Give the extent of all Plasmodium ovale-infected red blood cells.
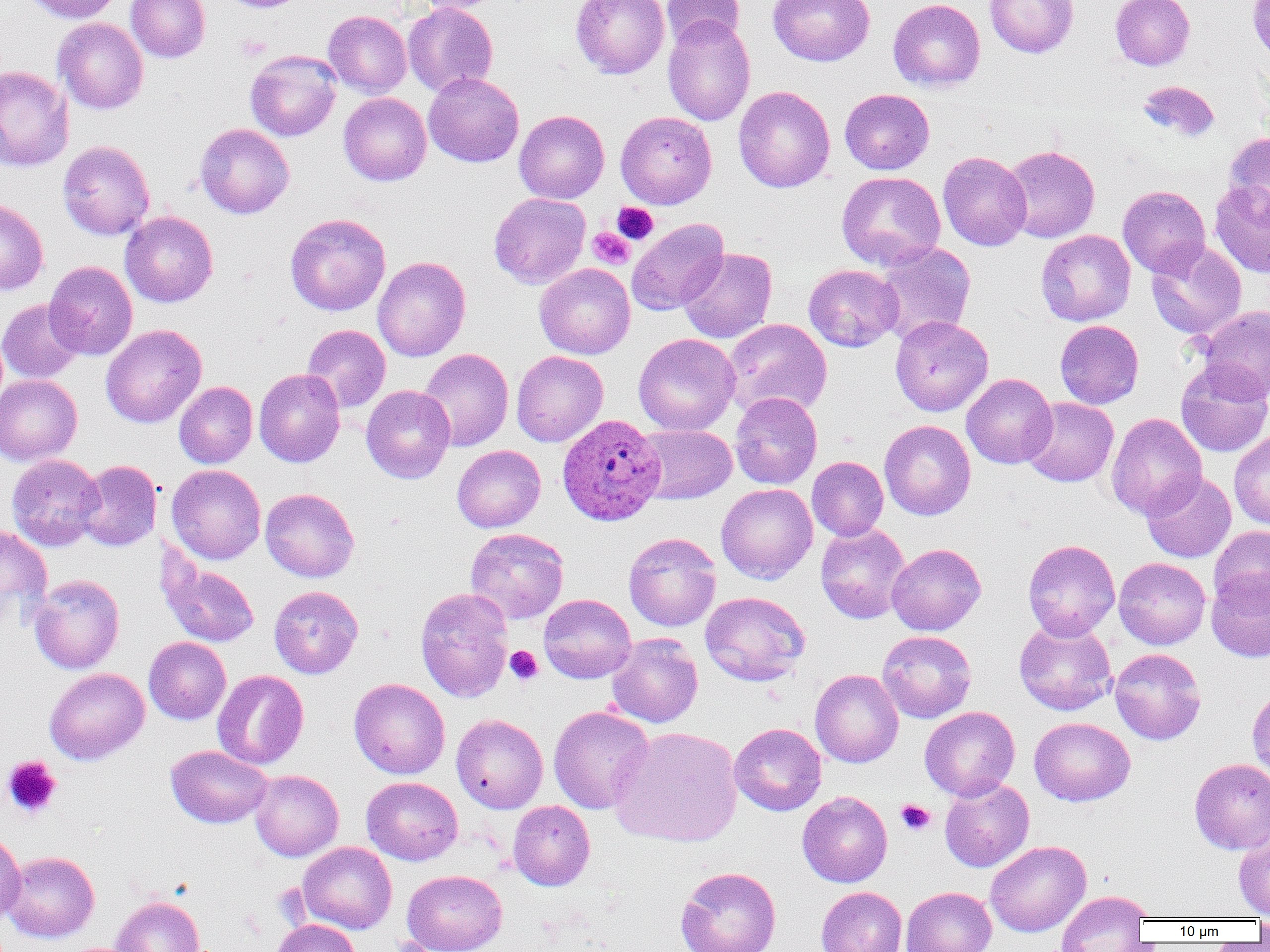

Approximate bounding boxes as (x1, y1, x2, y2) in pixels.
Plasmodium ovale-infected red blood cells: (557, 414, 665, 526).

slide-level diagnosis = Plasmodium ovale
magnification = 1000x
modality = optical microscopy
platelet locations = approximate bounding boxes as (x1, y1, x2, y2) in pixels: (235, 34, 271, 62), (612, 202, 658, 244), (588, 227, 634, 268), (504, 645, 543, 685), (2, 755, 62, 819), (896, 799, 935, 835)
field of view = single
uninfected red blood cell locations = approximate bounding boxes as (x1, y1, x2, y2) in pixels: (21, 0, 123, 23), (126, 0, 210, 62), (218, 0, 310, 13), (413, 0, 509, 14), (571, 0, 669, 79), (662, 0, 745, 50), (768, 0, 875, 66), (888, 0, 985, 91), (984, 0, 1079, 58), (1110, 0, 1195, 70), (1247, 0, 1270, 64), (402, 2, 498, 97), (323, 10, 412, 97), (662, 16, 755, 126), (52, 18, 149, 114), (245, 50, 341, 141), (0, 65, 74, 173), (423, 72, 524, 168), (1137, 80, 1220, 142), (734, 85, 835, 193), (839, 88, 934, 175), (338, 93, 431, 185), (514, 110, 609, 204), (615, 110, 717, 209), (195, 123, 294, 218), (1224, 131, 1270, 217), (58, 140, 155, 240), (1001, 145, 1100, 243), (938, 151, 1032, 251), (837, 171, 946, 271), (1210, 181, 1270, 276), (1118, 185, 1211, 278), (489, 192, 590, 289), (0, 198, 48, 295), (120, 211, 218, 307), (284, 213, 391, 315), (626, 218, 728, 315), (1036, 229, 1136, 326), (1146, 240, 1246, 339), (875, 242, 976, 346), (678, 248, 777, 343), (372, 257, 471, 361), (44, 261, 137, 360), (534, 263, 635, 359), (803, 264, 903, 352), (0, 298, 84, 384), (1198, 306, 1270, 403), (890, 315, 993, 416), (888, 316, 980, 520), (723, 319, 832, 418), (1055, 320, 1144, 409), (101, 324, 207, 428), (302, 324, 390, 412), (633, 333, 740, 436), (418, 348, 513, 451), (511, 351, 608, 447), (1175, 363, 1270, 457), (254, 368, 345, 467), (962, 374, 1058, 468), (0, 375, 82, 465), (174, 381, 257, 468), (361, 385, 455, 483), (730, 392, 822, 490), (1021, 397, 1119, 487), (1106, 412, 1206, 519), (879, 419, 976, 520), (635, 424, 737, 505), (1229, 431, 1270, 530), (452, 445, 545, 532), (6, 454, 104, 551), (807, 456, 889, 541), (75, 460, 162, 551), (166, 464, 266, 564), (1141, 471, 1236, 563), (716, 483, 818, 583), (260, 488, 359, 583), (816, 523, 910, 624), (0, 524, 52, 627), (1209, 525, 1270, 611), (465, 527, 569, 624), (624, 532, 722, 632), (1022, 539, 1120, 641), (886, 543, 986, 635), (156, 553, 260, 648), (1114, 557, 1210, 650), (1206, 569, 1270, 663), (29, 574, 124, 674), (268, 585, 363, 678), (415, 587, 514, 703), (700, 591, 810, 685), (538, 594, 636, 683), (1013, 619, 1117, 715), (877, 630, 976, 723), (607, 634, 703, 728), (144, 637, 231, 724), (1110, 648, 1206, 744), (44, 668, 149, 765), (212, 669, 308, 769), (810, 669, 903, 768), (349, 678, 450, 779), (1247, 684, 1270, 782), (549, 706, 654, 814), (920, 706, 1020, 801), (451, 713, 548, 813), (1029, 717, 1135, 806), (729, 723, 826, 816), (610, 726, 742, 847), (166, 745, 272, 828), (1189, 758, 1270, 854), (250, 769, 343, 861), (362, 776, 462, 865), (939, 777, 1034, 872), (797, 791, 892, 888), (508, 800, 595, 891), (0, 829, 26, 925), (1234, 830, 1270, 918), (985, 840, 1091, 937), (297, 841, 397, 933), (2, 851, 100, 942), (675, 866, 781, 952), (402, 870, 507, 952), (816, 886, 907, 952), (901, 886, 997, 952), (1055, 890, 1153, 951), (112, 895, 205, 952), (1254, 916, 1270, 941), (273, 920, 361, 952)
preparation = thin blood film
image size = 1270×952 pixels